Classify this cell by malaria status.
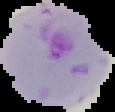

Parasitized.

preparation = thin blood smear
image type = cell region segmented out of the field of view; surrounding area masked to black
image size = 115×112 pixels